State which parasite is depicted.
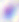
Toxoplasma gondii.

{
  "modality": "photomicrograph",
  "magnification": "400x"
}